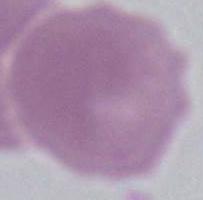 An erythrocyte is shown. Micrograph. Captured at 1000x magnification.